Assess the morphology of the erythrocytes.
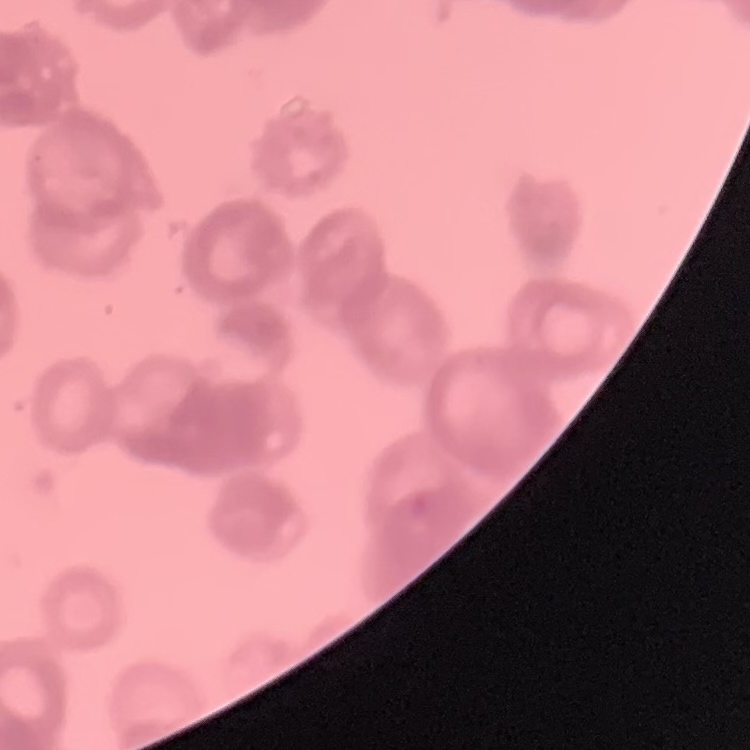

Rouleaux formation.

Summary:
  - Preparation: thin blood film
  - Image type: one tile cut from a larger photomicrograph
  - Stain: Field's or Giemsa